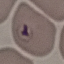

malaria status = uninfected
preparation = thin blood smear
stain = Giemsa
capture = smartphone camera at the microscope eyepiece
image type = cell patch, automatically extracted from a larger field of view and resized to 64 × 64 pixels